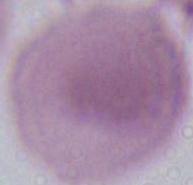
Photomicrograph. Captured at 1000x magnification. A red blood cell is seen.